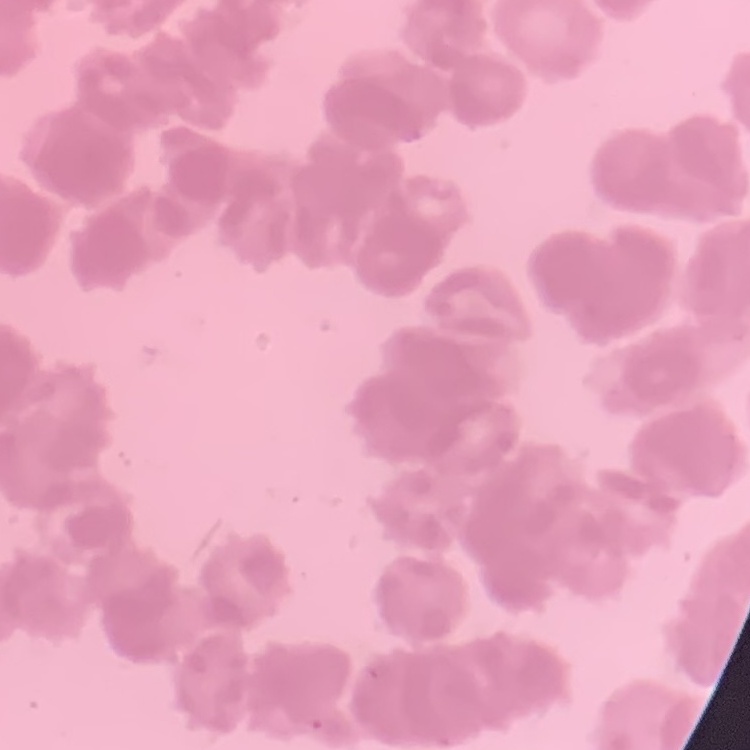

Summary:
  - Red blood cell morphology: rouleaux formation
  - Stain: Field's or Giemsa
  - Image type: square crop of a larger photomicrograph
  - Preparation: thin peripheral smear